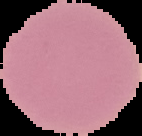
Cell region segmented out of the field of view; the surrounding area is masked to black. From a thin blood smear. Malaria status: uninfected. Image is 142×136 pixels.